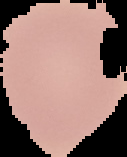
Summary:
  - Preparation: thin blood film
  - Image type: segmented cell region with the area outside set to black
  - Image size: 127×157 pixels
  - Malaria status: uninfected